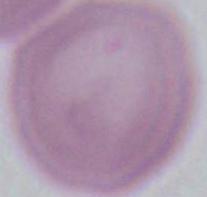

Photomicrograph. A red blood cell is seen. Captured at 1000x magnification.